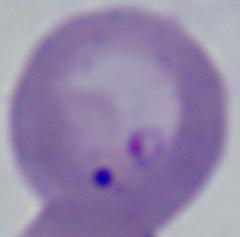

{
  "modality": "micrograph",
  "identification": "Babesia",
  "magnification": "1000x"
}